State which parasite is depicted.
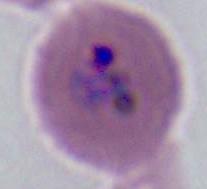

Plasmodium.

Captured at either 400x or 1000x magnification. Micrograph.